Classify this cell by malaria status.
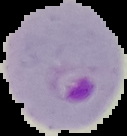
It is parasitized.

The area outside the segmented cell region is set to black. Image is 127×136 pixels. From a thin blood film.